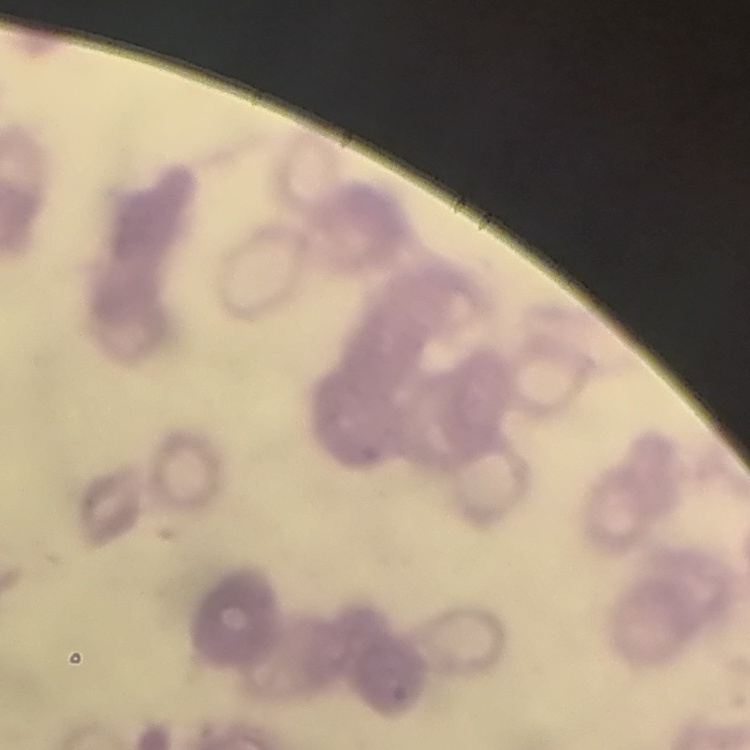
Summary:
  - Erythrocyte morphology: rouleaux formation
  - Preparation: thin blood film
  - Image type: square crop of a larger photomicrograph
  - Stain: Field's or Giemsa